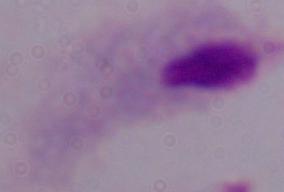
Photomicrograph. 1000x magnification. A trichomonad is shown.